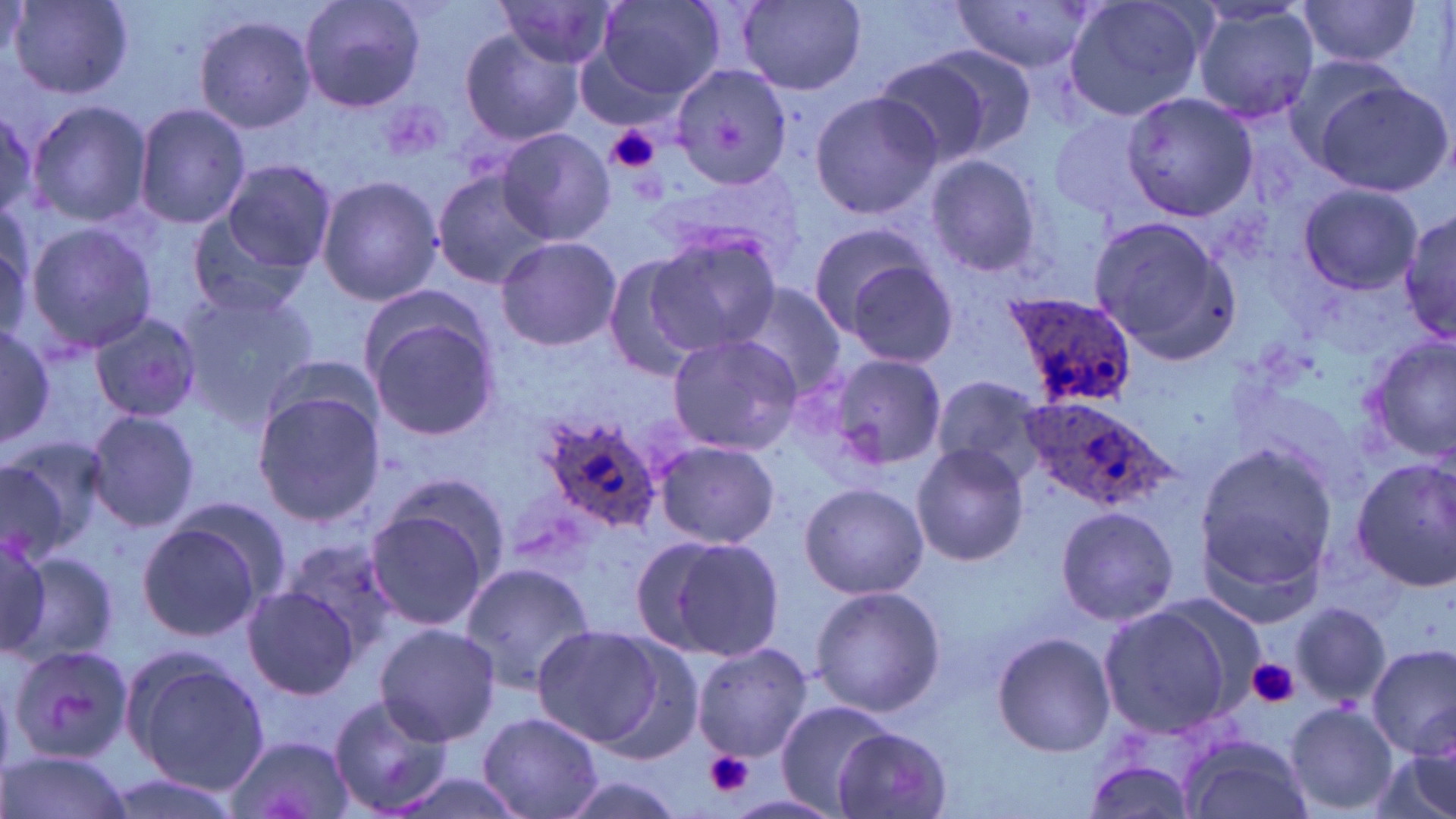
slide_level_diagnosis: Plasmodium ovale
stain: May-Grünwald-Giemsa
plasmodium_ovale_infected_red_blood_cell_locations: 'approximate bounding boxes as [x1, y1, x2, y2] in pixels: [997, 290, 1140, 412], [1016, 395, 1174, 512], [534, 413, 667, 534]'
field_of_view: one of a larger specimen
uninfected_red_blood_cell_locations: 'approximate bounding boxes as [x1, y1, x2, y2] in pixels: [299, 0, 426, 113], [590, 0, 727, 104], [1058, 0, 1212, 122], [6, 1, 133, 99], [735, 1, 866, 93], [952, 1, 1100, 73], [1296, 1, 1426, 68], [492, 2, 622, 71], [1190, 3, 1321, 126], [194, 12, 318, 132], [457, 28, 585, 146], [914, 42, 1039, 158], [1280, 52, 1423, 172], [871, 57, 993, 168], [668, 63, 793, 189], [1312, 80, 1453, 198], [806, 89, 943, 219], [1121, 91, 1260, 222], [27, 101, 152, 228], [134, 102, 251, 230], [0, 103, 37, 225], [1050, 109, 1161, 219], [496, 127, 614, 245], [923, 154, 1046, 279], [219, 158, 336, 274], [431, 170, 557, 289], [316, 174, 443, 306], [1299, 184, 1423, 295], [1399, 205, 1454, 348], [1085, 215, 1241, 361], [185, 216, 312, 319], [804, 219, 943, 338], [23, 221, 157, 356], [644, 227, 782, 357], [495, 235, 622, 350], [835, 250, 959, 368], [601, 255, 709, 381], [731, 284, 847, 398], [174, 285, 320, 421], [363, 301, 504, 444], [89, 314, 204, 423], [0, 319, 55, 454], [664, 333, 805, 456], [1365, 337, 1456, 461], [827, 352, 946, 471], [932, 373, 1048, 480], [250, 388, 384, 528], [84, 409, 201, 532], [656, 439, 778, 549], [0, 440, 104, 561], [911, 443, 1029, 566], [1195, 444, 1339, 587], [1351, 458, 1456, 593], [798, 481, 928, 600], [166, 494, 294, 610], [362, 499, 495, 636], [1057, 502, 1179, 627], [135, 518, 270, 642], [646, 533, 787, 661], [0, 539, 52, 658], [281, 540, 402, 656], [11, 547, 117, 669], [459, 559, 596, 691], [809, 584, 946, 717], [244, 585, 361, 700], [1289, 600, 1391, 709], [1096, 602, 1241, 739], [375, 623, 501, 747], [530, 624, 672, 751], [991, 631, 1116, 757], [586, 635, 707, 764], [693, 641, 812, 760], [1368, 644, 1454, 760], [5, 645, 130, 767], [122, 651, 267, 794], [327, 693, 454, 817], [773, 700, 894, 815], [1284, 703, 1397, 814], [478, 711, 602, 818], [834, 728, 953, 817], [224, 733, 355, 819], [1179, 734, 1312, 819], [1375, 735, 1456, 819], [1077, 741, 1217, 819], [2, 749, 131, 819], [376, 771, 532, 819], [554, 771, 689, 819], [94, 772, 246, 819]'
modality: optical microscopy
preparation: thin blood film
image_size: 1456×819 pixels
platelet_locations: 'approximate bounding boxes as [x1, y1, x2, y2] in pixels: [606, 124, 661, 175], [1246, 657, 1299, 707], [703, 752, 757, 799]'
magnification: 1000x